Give the position of each Plasmodium falciparum parasite with its life-cycle stage, each leukocyte, and any debris.
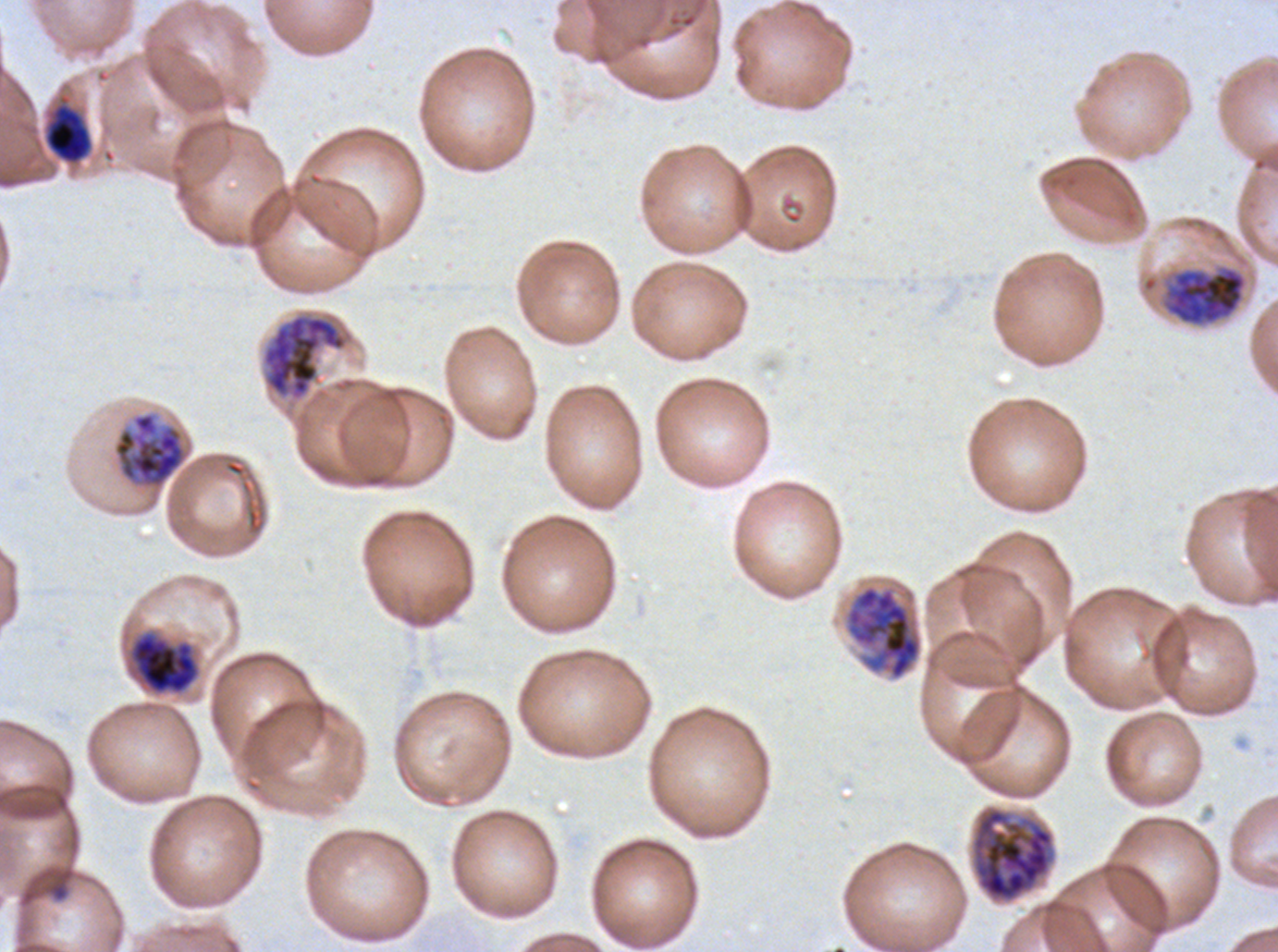
Approximate bounding boxes as [x1, y1, x2, y2] in pixels.
Rings: [49, 882, 68, 901].
Mid trophozoites: [45, 107, 91, 163].
Early schizonts: [1162, 265, 1247, 327], [113, 412, 186, 488], [130, 633, 199, 694].
Late schizonts: [263, 314, 347, 398], [844, 583, 923, 681], [970, 805, 1056, 903].
No late-ring/early-trophozoite forms, late trophozoites, segmenters, gametocytes, leukocytes, or debris observed.

Thin blood film. Giemsa-stained preparation. Life-cycle stages observed: ring, mid trophozoite, early schizont, late schizont. Image is 1278×952 pixels. Ex-vivo Plasmodium falciparum culture from a patient in The Gambia, grown for 24 to 48 hours. One sub-image of a larger composite.